Assess this cell for malaria.
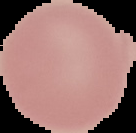
It is uninfected.

Summary:
  - Image size: 136×133 pixels
  - Image type: cell region segmented out of the field of view; surrounding area masked to black
  - Preparation: thin blood smear